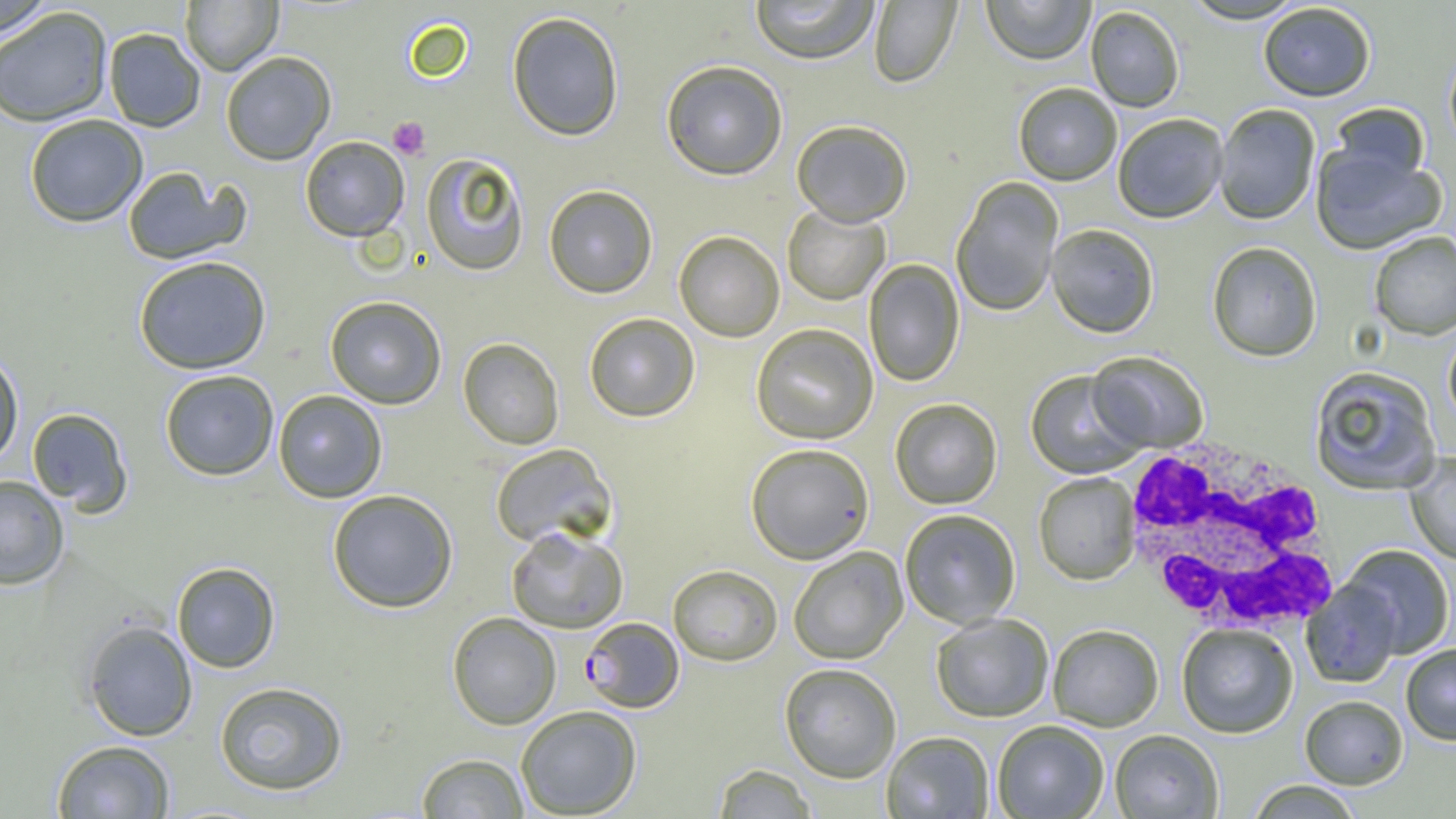

Summary:
  - Coordinate format: approximate bounding boxes as named x1/y1/x2/y2 corners in pixels
  - Platelet locations: (x1=388, y1=117, x2=430, y2=159)
  - White blood cell locations: (x1=1118, y1=437, x2=1342, y2=640)
  - Uninfected red blood cell locations: (x1=0, y1=0, x2=57, y2=38), (x1=180, y1=0, x2=282, y2=75), (x1=749, y1=0, x2=880, y2=64), (x1=981, y1=0, x2=1096, y2=67), (x1=1180, y1=0, x2=1308, y2=25), (x1=869, y1=1, x2=962, y2=88), (x1=1259, y1=3, x2=1376, y2=102), (x1=1085, y1=6, x2=1185, y2=113), (x1=0, y1=7, x2=113, y2=127), (x1=507, y1=11, x2=625, y2=141), (x1=103, y1=28, x2=205, y2=132), (x1=1444, y1=45, x2=1456, y2=156), (x1=220, y1=51, x2=336, y2=165), (x1=660, y1=59, x2=788, y2=180), (x1=1013, y1=83, x2=1122, y2=187), (x1=1330, y1=103, x2=1431, y2=187), (x1=1214, y1=105, x2=1320, y2=226), (x1=24, y1=114, x2=148, y2=227), (x1=1113, y1=114, x2=1228, y2=225), (x1=791, y1=120, x2=913, y2=228), (x1=300, y1=136, x2=409, y2=241), (x1=1310, y1=144, x2=1448, y2=257), (x1=420, y1=152, x2=531, y2=276), (x1=122, y1=166, x2=249, y2=265), (x1=951, y1=177, x2=1064, y2=318), (x1=543, y1=184, x2=658, y2=298), (x1=782, y1=204, x2=891, y2=306), (x1=1046, y1=225, x2=1159, y2=339), (x1=674, y1=231, x2=785, y2=342), (x1=1369, y1=231, x2=1456, y2=341), (x1=1207, y1=243, x2=1321, y2=362), (x1=133, y1=256, x2=272, y2=374), (x1=864, y1=259, x2=965, y2=388), (x1=324, y1=295, x2=447, y2=409), (x1=584, y1=313, x2=700, y2=422), (x1=750, y1=324, x2=878, y2=445), (x1=1443, y1=328, x2=1456, y2=431), (x1=458, y1=338, x2=564, y2=449), (x1=0, y1=348, x2=24, y2=469), (x1=1085, y1=351, x2=1208, y2=453), (x1=1309, y1=366, x2=1442, y2=496), (x1=159, y1=369, x2=279, y2=480), (x1=1025, y1=371, x2=1147, y2=479), (x1=273, y1=390, x2=387, y2=503), (x1=889, y1=399, x2=1003, y2=510), (x1=26, y1=407, x2=132, y2=513), (x1=489, y1=443, x2=616, y2=549), (x1=745, y1=444, x2=875, y2=564), (x1=1404, y1=453, x2=1456, y2=565), (x1=1033, y1=473, x2=1140, y2=586), (x1=0, y1=475, x2=69, y2=590), (x1=327, y1=489, x2=459, y2=613), (x1=899, y1=509, x2=1021, y2=629), (x1=506, y1=525, x2=629, y2=633), (x1=1340, y1=545, x2=1455, y2=659), (x1=788, y1=547, x2=907, y2=665), (x1=171, y1=562, x2=280, y2=673), (x1=667, y1=564, x2=783, y2=666), (x1=1302, y1=580, x2=1403, y2=689), (x1=447, y1=612, x2=562, y2=729), (x1=931, y1=613, x2=1054, y2=723), (x1=81, y1=619, x2=198, y2=741), (x1=1177, y1=624, x2=1298, y2=739), (x1=1048, y1=625, x2=1164, y2=732), (x1=1401, y1=644, x2=1456, y2=745), (x1=778, y1=663, x2=902, y2=783), (x1=214, y1=681, x2=348, y2=795), (x1=1300, y1=695, x2=1408, y2=789), (x1=515, y1=705, x2=642, y2=818), (x1=992, y1=721, x2=1109, y2=818), (x1=1109, y1=730, x2=1224, y2=819), (x1=882, y1=731, x2=994, y2=818), (x1=51, y1=740, x2=175, y2=818), (x1=416, y1=753, x2=529, y2=818), (x1=712, y1=764, x2=817, y2=818), (x1=1246, y1=780, x2=1364, y2=819)
  - Plasmodium falciparum-infected red blood cell locations: (x1=580, y1=617, x2=684, y2=713)
  - Slide-level diagnosis: Plasmodium falciparum
  - Modality: light microscopy
  - Magnification: 1000x
  - Preparation: thin blood film
  - Image size: 1456×819 pixels
  - Field of view: single